Locate every leukocyte (white blood cell).
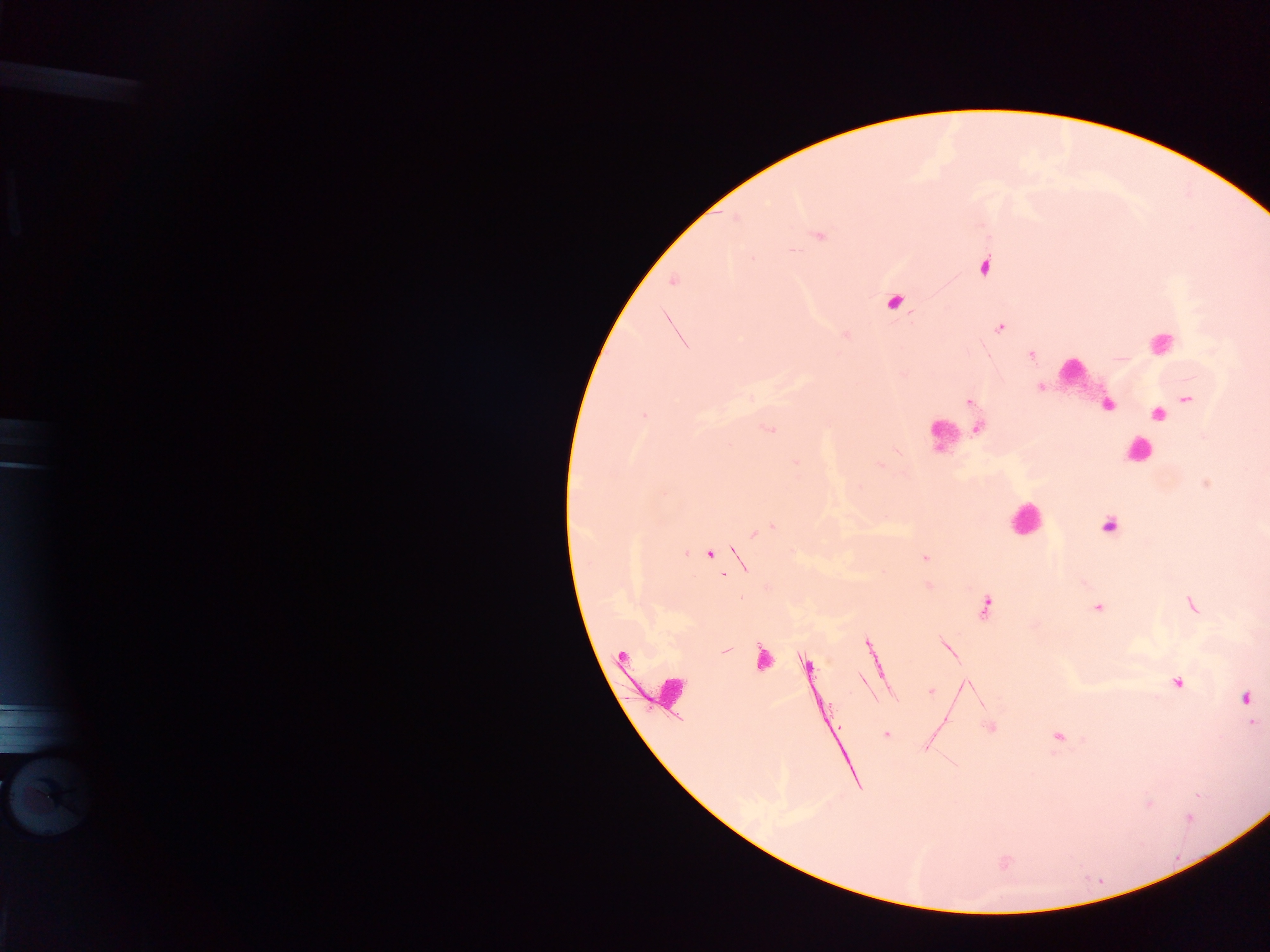
Approximate centers as x y in pixels.
Leukocytes: 1160 342; 1072 372; 945 434; 1137 451; 1025 519; 669 693; 50 793.

plasmodium_parasite_locations: 'approximate centers as x y in pixels: 820 237; 983 267; 673 282; 893 303; 999 328; 1032 356; 1040 387; 1188 399; 969 402; 1107 405; 1158 414; 644 415; 978 429; 769 430; 796 462; 1206 484; 1109 526; 757 532; 709 554; 924 558; 986 605; 1192 605; 1098 608; 868 645; 725 651; 761 658; 806 666; 863 680; 1178 683; 931 691; 1245 698; 1253 722; 990 727; 886 734; 1058 737; 1189 817'
capture: mobile-phone photograph through a microscope
preparation: thick blood film
image_size: 1270×952 pixels
country: Ghana
field_of_view: single